Give the extent of all uninfected red blood cells.
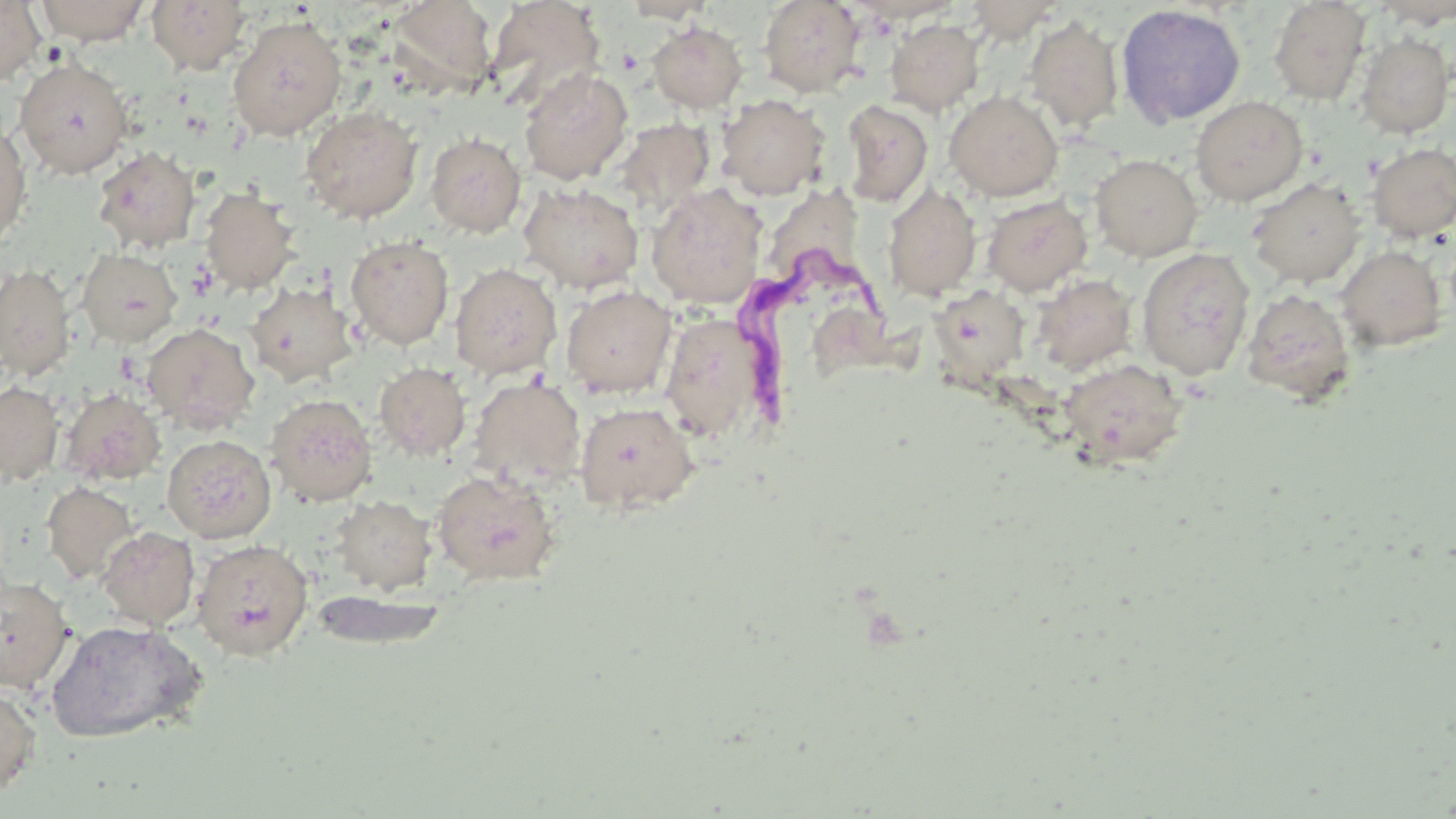

Approximate bounding boxes as [x1, y1, x2, y2] in pixels.
Uninfected red blood cells: [36, 0, 149, 45], [147, 0, 251, 75], [486, 0, 605, 110], [619, 0, 718, 23], [757, 0, 865, 97], [0, 1, 45, 86], [387, 1, 497, 96], [962, 1, 1065, 42], [1268, 1, 1371, 106], [1369, 1, 1456, 28], [1115, 4, 1246, 128], [227, 15, 347, 141], [1023, 15, 1124, 132], [884, 18, 985, 115], [647, 21, 748, 113], [1355, 33, 1454, 138], [14, 57, 133, 179], [519, 67, 633, 184], [944, 90, 1064, 201], [716, 94, 831, 199], [1190, 96, 1308, 205], [840, 100, 933, 208], [300, 105, 424, 224], [615, 118, 715, 214], [0, 122, 32, 249], [425, 132, 526, 237], [1366, 142, 1456, 242], [92, 146, 202, 253], [1090, 153, 1202, 261], [1247, 177, 1366, 288], [765, 178, 873, 275], [518, 182, 643, 293], [646, 183, 767, 308], [882, 183, 982, 301], [199, 188, 300, 294], [982, 195, 1092, 295], [345, 235, 454, 349], [1336, 245, 1447, 352], [1136, 247, 1255, 380], [77, 248, 182, 347], [0, 263, 77, 382], [450, 263, 562, 379], [1032, 274, 1136, 374], [245, 281, 347, 387], [561, 286, 676, 398], [930, 287, 1029, 382], [1240, 288, 1357, 408], [659, 314, 771, 442], [142, 323, 260, 434], [1057, 359, 1190, 472], [375, 363, 470, 461], [470, 377, 586, 489], [0, 381, 63, 485], [60, 388, 165, 486], [266, 394, 378, 506], [574, 402, 699, 515], [162, 435, 277, 543], [431, 469, 561, 586], [42, 482, 139, 585], [331, 495, 436, 595], [97, 526, 200, 629], [192, 538, 313, 660], [0, 575, 74, 693], [310, 589, 448, 650], [45, 619, 207, 744], [0, 684, 42, 799].

Trypanosoma brucei locations: [737, 241, 883, 432]. Slide-level diagnosis: Trypanosoma brucei. Thin blood smear. Captured at 1000x magnification. Image is 1456×819 pixels. Single field of view. May-Grünwald-Giemsa-stained preparation. Optical microscopy.